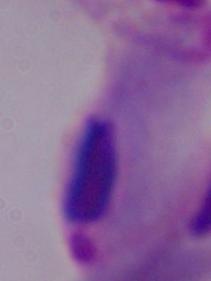
{
  "magnification": "1000x",
  "identification": "trichomonad",
  "modality": "micrograph"
}